Report the malaria status of this cell.
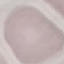
Uninfected.

Summary:
  - Capture: smartphone camera at the microscope eyepiece
  - Preparation: thin smear
  - Image type: automatically extracted cell patch, resized to 64 × 64 pixels
  - Stain: Giemsa